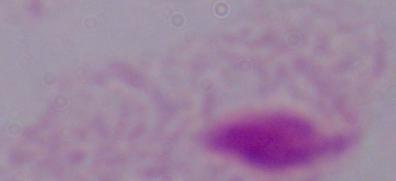

identification: trichomonad
modality: micrograph
magnification: 1000x